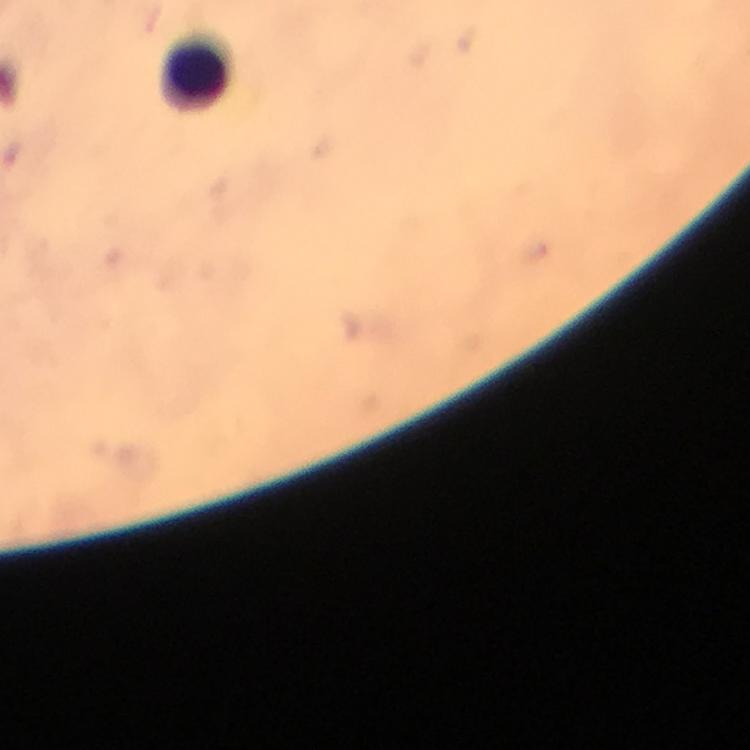

Approximate centers as (x, y) in pixels.
Summary:
  - Leukocyte locations: (197, 72)
  - Immersion oil: used
  - Stain: Giemsa
  - Context: from a malaria diagnostic workup
  - Preparation: thick blood film
  - Image size: 750×750 pixels
  - Magnification: 100x
  - Capture: smartphone mounted on the microscope
  - Cropped from: one field of view
  - Malaria parasites: none detected